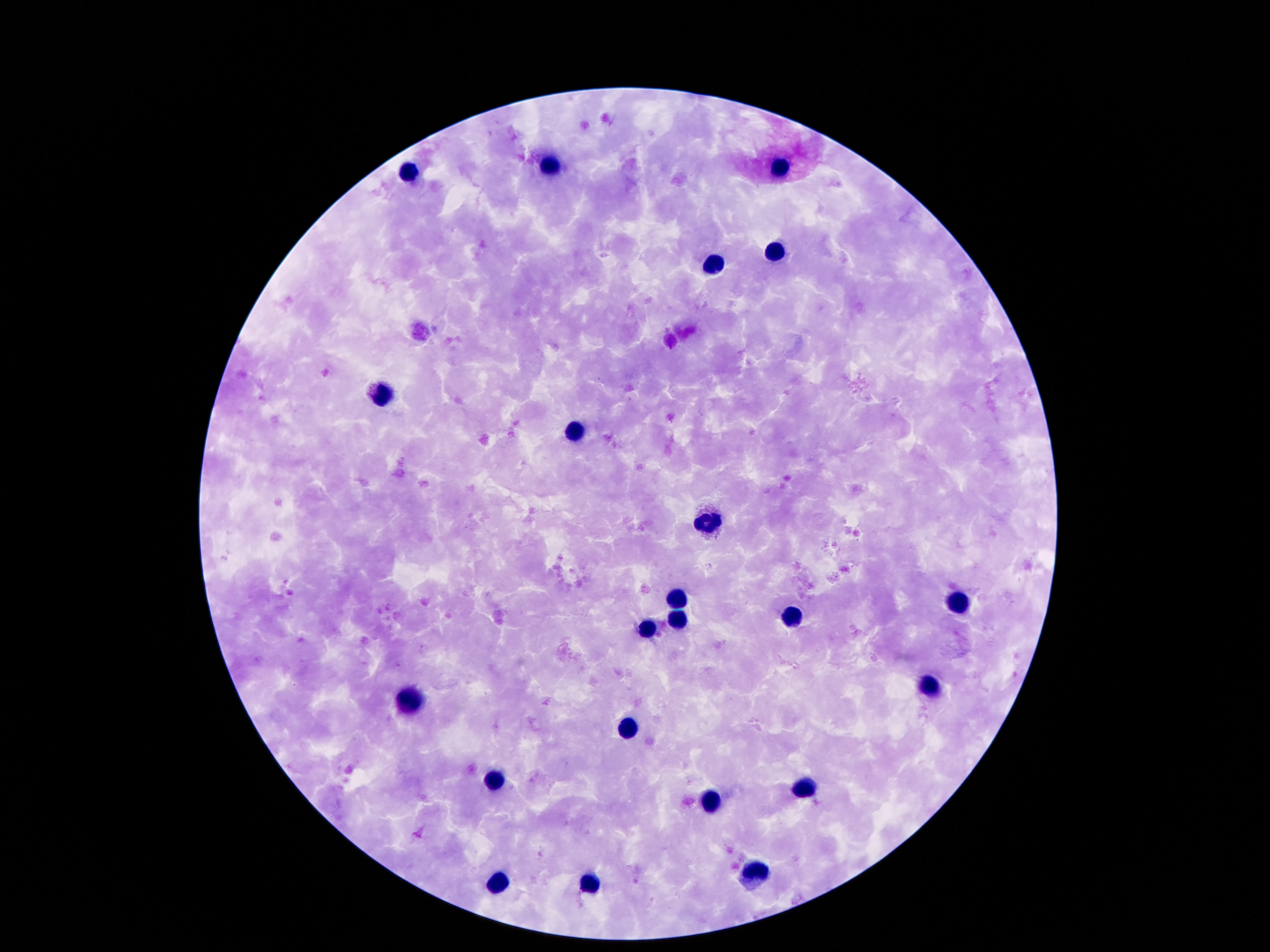

image size = 1270×952 pixels
preparation = thick blood smear
magnification = 100x
capture = smartphone camera through the microscope eyepiece
patient malaria status = not infected
leukocyte locations = approximate centers as [x, y] in pixels: [553, 165], [780, 167], [406, 171], [776, 251], [714, 264], [381, 395], [574, 433], [706, 524], [677, 601], [957, 605], [792, 617], [680, 620], [648, 629], [929, 689], [412, 700], [627, 729], [494, 778], [806, 788], [709, 800], [756, 873], [498, 883], [590, 886]
field of view = one from this slide
stain = Giemsa